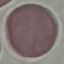

Malaria status: uninfected. Cell patch, automatically extracted from a larger field of view and resized to 64 × 64 pixels. Acquired by smartphone through the microscope eyepiece. Giemsa stain. Thin blood film.